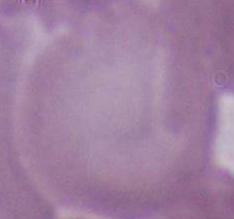

Summary:
  - Identification: red blood cell
  - Modality: photomicrograph
  - Magnification: 1000x